Assess the morphology of the erythrocytes.
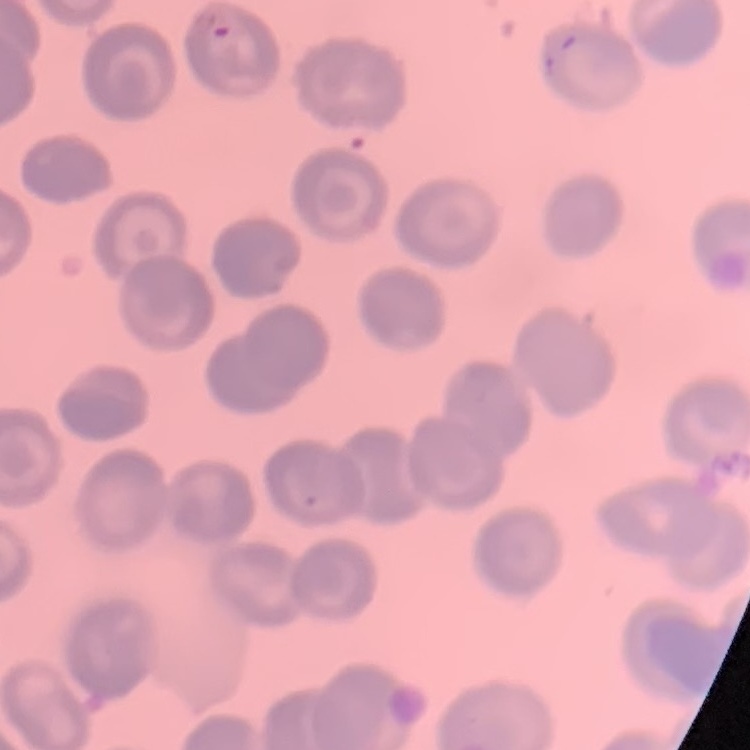
No rouleaux formation.

{
  "image_type": "square crop of a larger photomicrograph",
  "stain": "Field's or Giemsa",
  "preparation": "thin blood film"
}